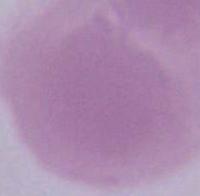

{
  "magnification": "1000x",
  "modality": "photomicrograph",
  "identification": "erythrocyte"
}